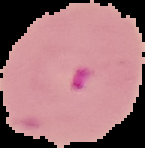

result: Plasmodium parasites identified
preparation: thin blood smear
image_size: 145×148 pixels
image_type: cell region segmented out of the field of view; surrounding area masked to black